State the preparation type.
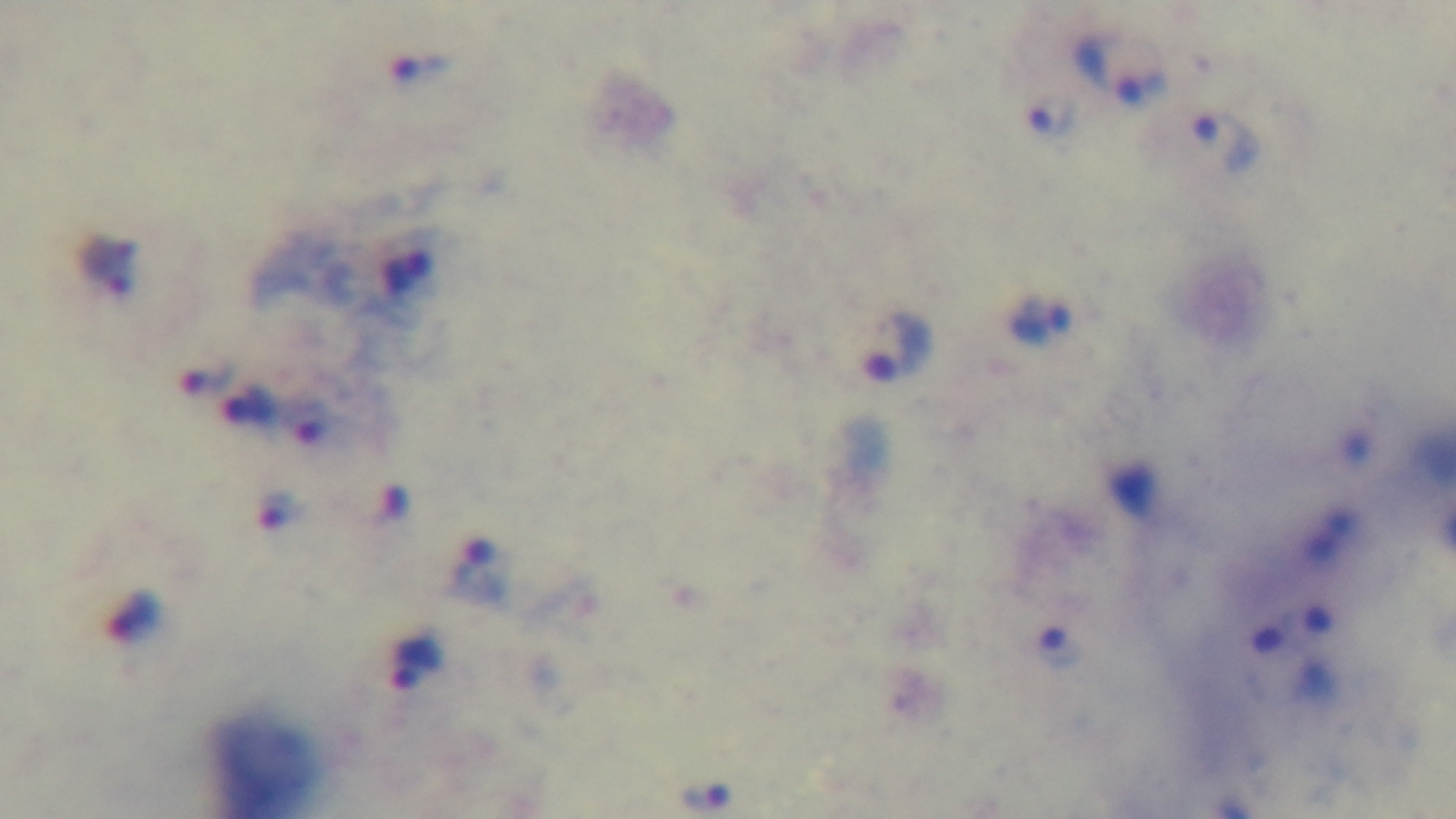

A thick smear.

Summary:
  - Modality: light microscopy
  - Field of view: single
  - Capture: mounted 4K digital camera
  - Stain: Giemsa
  - Objective: 100x oil immersion
  - Malaria status: infected